Identify the parasite.
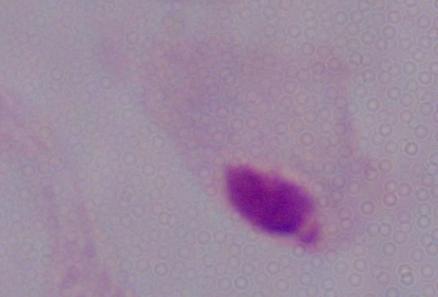

This is a trichomonad.

{
  "magnification": "1000x",
  "modality": "micrograph"
}